Outline each blood parasite and name the species.
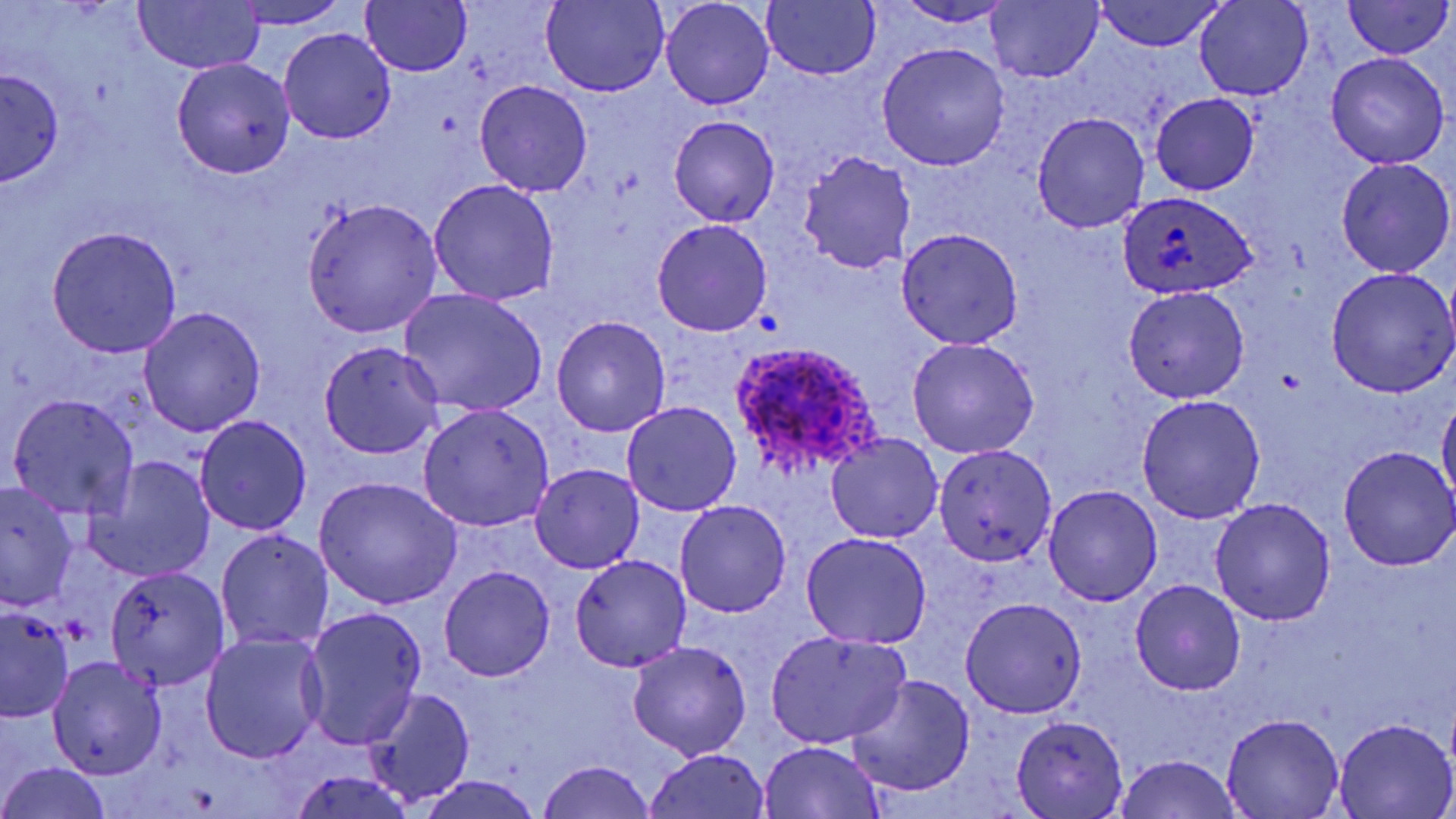

Approximate bounding boxes as named x1/y1/x2/y2 corners in pixels.
Plasmodium ovale-infected red blood cells: (x1=1117, y1=190, x2=1258, y2=299), (x1=726, y1=341, x2=888, y2=482).
No Plasmodium falciparum, Plasmodium malariae, Plasmodium vivax, Babesia divergens, or Trypanosoma brucei observed.

slide-level diagnosis = Plasmodium ovale
uninfected red blood cell locations = approximate bounding boxes as named x1/y1/x2/y2 corners in pixels: (x1=134, y1=0, x2=265, y2=74), (x1=988, y1=0, x2=1104, y2=83), (x1=1343, y1=0, x2=1451, y2=61), (x1=228, y1=1, x2=351, y2=29), (x1=359, y1=1, x2=472, y2=77), (x1=762, y1=1, x2=881, y2=80), (x1=1096, y1=1, x2=1226, y2=52), (x1=1193, y1=1, x2=1313, y2=100), (x1=540, y1=2, x2=669, y2=96), (x1=660, y1=2, x2=775, y2=109), (x1=893, y1=2, x2=1016, y2=25), (x1=278, y1=28, x2=396, y2=145), (x1=878, y1=43, x2=1011, y2=170), (x1=1326, y1=51, x2=1450, y2=168), (x1=171, y1=58, x2=296, y2=179), (x1=0, y1=66, x2=64, y2=186), (x1=474, y1=79, x2=593, y2=197), (x1=1152, y1=93, x2=1258, y2=195), (x1=1033, y1=112, x2=1150, y2=233), (x1=668, y1=114, x2=779, y2=228), (x1=798, y1=149, x2=916, y2=273), (x1=1335, y1=157, x2=1455, y2=278), (x1=428, y1=179, x2=559, y2=306), (x1=301, y1=198, x2=443, y2=338), (x1=652, y1=217, x2=773, y2=337), (x1=47, y1=228, x2=182, y2=357), (x1=894, y1=228, x2=1022, y2=349), (x1=1326, y1=267, x2=1456, y2=398), (x1=1124, y1=286, x2=1250, y2=404), (x1=400, y1=289, x2=549, y2=418), (x1=139, y1=306, x2=266, y2=436), (x1=551, y1=317, x2=671, y2=437), (x1=907, y1=337, x2=1040, y2=459), (x1=318, y1=342, x2=445, y2=459), (x1=1438, y1=391, x2=1456, y2=509), (x1=9, y1=393, x2=139, y2=518), (x1=1135, y1=395, x2=1264, y2=523), (x1=622, y1=401, x2=741, y2=515), (x1=417, y1=403, x2=554, y2=531), (x1=194, y1=414, x2=312, y2=536), (x1=825, y1=432, x2=943, y2=542), (x1=933, y1=443, x2=1057, y2=566), (x1=1338, y1=447, x2=1456, y2=570), (x1=86, y1=457, x2=215, y2=582), (x1=530, y1=463, x2=644, y2=573), (x1=314, y1=477, x2=462, y2=610), (x1=1, y1=480, x2=80, y2=611), (x1=1044, y1=485, x2=1162, y2=607), (x1=1209, y1=498, x2=1335, y2=626), (x1=674, y1=500, x2=791, y2=617), (x1=216, y1=528, x2=335, y2=652), (x1=800, y1=532, x2=933, y2=651), (x1=568, y1=555, x2=691, y2=672), (x1=440, y1=565, x2=555, y2=682), (x1=104, y1=566, x2=231, y2=690), (x1=1131, y1=580, x2=1246, y2=695), (x1=960, y1=596, x2=1087, y2=717), (x1=0, y1=604, x2=75, y2=720), (x1=300, y1=605, x2=427, y2=751), (x1=764, y1=630, x2=912, y2=749), (x1=197, y1=631, x2=327, y2=764), (x1=628, y1=640, x2=752, y2=762), (x1=46, y1=655, x2=167, y2=781), (x1=846, y1=675, x2=976, y2=798), (x1=363, y1=689, x2=477, y2=808), (x1=1011, y1=715, x2=1126, y2=818), (x1=1220, y1=715, x2=1344, y2=818), (x1=1331, y1=718, x2=1455, y2=819), (x1=759, y1=741, x2=887, y2=819), (x1=644, y1=748, x2=773, y2=819), (x1=1113, y1=754, x2=1244, y2=819), (x1=536, y1=761, x2=658, y2=819), (x1=1, y1=763, x2=114, y2=819), (x1=287, y1=767, x2=418, y2=819), (x1=412, y1=776, x2=547, y2=819)
modality = light microscopy
field of view = one of a larger specimen
preparation = thin blood smear
magnification = 1000x
stain = May-Grünwald-Giemsa
image size = 1456×819 pixels